Report the malaria status of this cell.
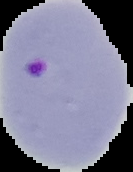

It is parasitized.

Summary:
  - Image size: 133×172 pixels
  - Image type: cell region segmented out of the field of view; surrounding area masked to black
  - Preparation: thin blood smear